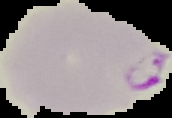

preparation = thin blood smear
image type = segmented cell region with the area outside set to black
malaria status = parasitized
image size = 172×118 pixels